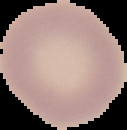
Summary:
  - Result: no Plasmodium parasites detected
  - Image size: 127×130 pixels
  - Preparation: thin blood smear
  - Image type: segmented cell region with the area outside set to black